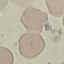

Result: no malaria parasites seen. Thin blood film. Acquired by smartphone through the microscope eyepiece. Cell patch, automatically extracted from a larger field of view and resized to 64 × 64 pixels. Giemsa stain.